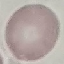
Summary:
  - Malaria status: uninfected
  - Image type: automatically extracted cell patch, resized to 64 × 64 pixels
  - Capture: smartphone camera at the microscope eyepiece
  - Stain: Giemsa
  - Preparation: thin blood film